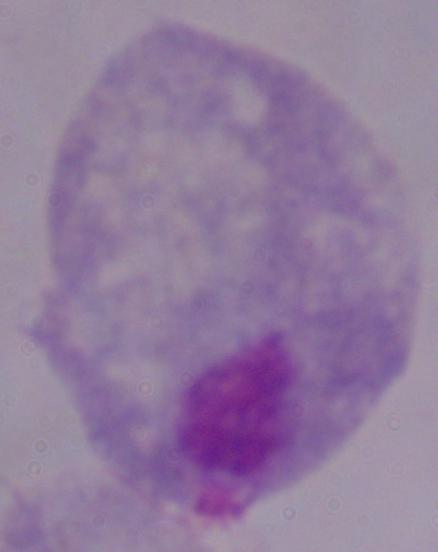
1000x magnification. Micrograph. A trichomonad is seen.